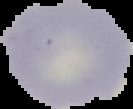

Summary:
  - Malaria status: uninfected
  - Image size: 133×109 pixels
  - Preparation: thin blood film
  - Image type: cell region segmented out of the field of view; surrounding area masked to black